Describe the morphology of the red blood cells.
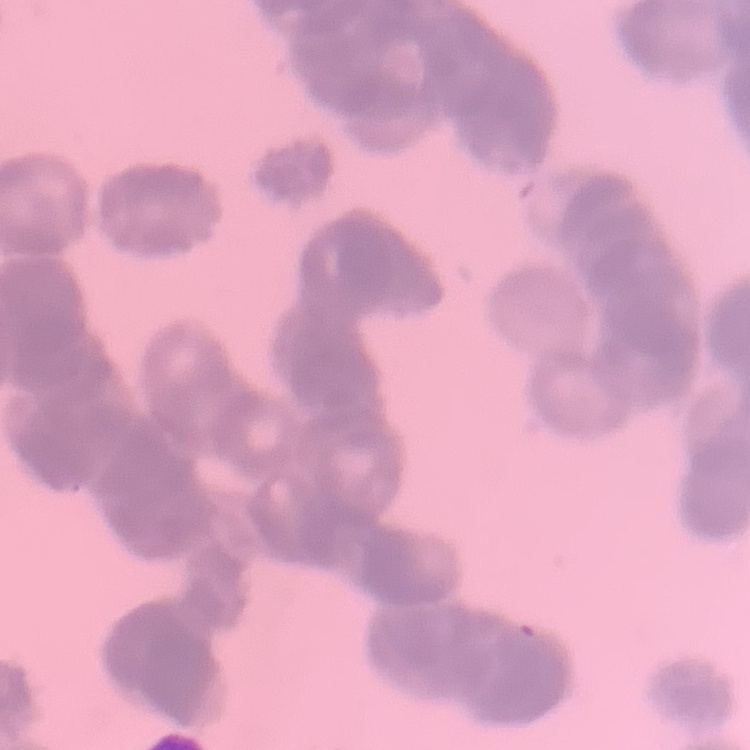

They show rouleaux formation.

One tile cut from a larger photomicrograph. Thin blood film. Field's or Giemsa stain.